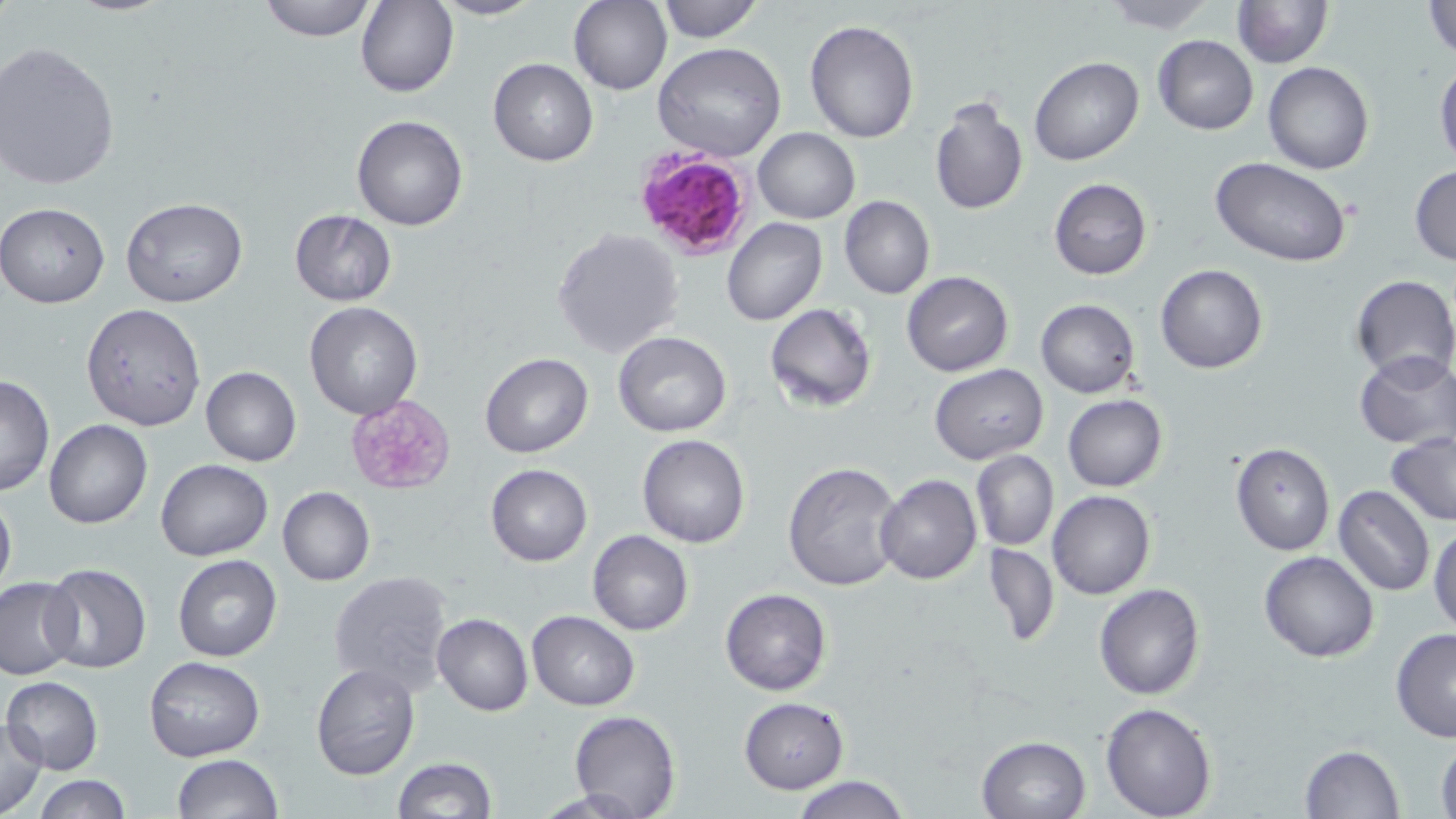
Summary:
  - Coordinate format: approximate bounding boxes as (x1,y1)-(x2,y2) corner pairs in pixels
  - Platelet locations: (345,393)-(457,492)
  - Uninfected red blood cell locations: (258,0)-(379,41), (433,0)-(542,21), (569,0)-(672,95), (656,0)-(762,42), (1096,0)-(1222,32), (1232,0)-(1332,68), (357,1)-(458,98), (1424,1)-(1454,58), (804,19)-(920,143), (1152,35)-(1258,136), (0,41)-(122,191), (652,43)-(787,163), (1029,57)-(1143,167), (487,58)-(598,166), (1435,59)-(1456,170), (1263,62)-(1374,176), (928,94)-(1028,217), (351,115)-(468,231), (752,129)-(859,224), (1209,157)-(1355,271), (1409,164)-(1456,266), (1049,178)-(1151,280), (840,196)-(935,299), (121,197)-(248,308), (1,202)-(109,308), (289,210)-(396,305), (721,217)-(827,327), (552,227)-(684,360), (1155,263)-(1267,373), (902,272)-(1013,375), (1350,274)-(1455,384), (1035,300)-(1141,400), (304,302)-(423,420), (80,303)-(207,432), (765,303)-(877,412), (613,332)-(732,437), (479,352)-(594,458), (1354,352)-(1456,450), (931,364)-(1048,465), (200,366)-(302,466), (0,375)-(54,497), (1063,394)-(1167,491), (44,420)-(152,529), (1385,433)-(1456,526), (638,434)-(749,548), (1231,443)-(1334,556), (970,449)-(1059,550), (156,459)-(272,560), (782,460)-(904,592), (486,464)-(593,566), (876,474)-(982,585), (1334,485)-(1434,596), (0,487)-(16,604), (277,487)-(375,586), (1048,490)-(1155,600), (1429,523)-(1456,635), (587,529)-(694,636), (983,541)-(1060,647), (1259,551)-(1379,662), (172,554)-(282,662), (37,564)-(153,675), (327,570)-(455,696), (0,577)-(80,677), (1094,583)-(1206,699), (720,588)-(832,695), (527,610)-(641,710), (432,613)-(532,716), (1390,629)-(1456,742), (144,655)-(266,762), (310,663)-(421,780), (2,676)-(103,774), (738,696)-(850,794), (1100,702)-(1217,818), (570,710)-(678,819), (0,717)-(48,818), (1435,732)-(1456,819), (977,735)-(1091,819), (1298,744)-(1404,819), (171,753)-(284,819), (390,757)-(497,818), (31,775)-(133,818), (792,775)-(909,819)
  - Plasmodium falciparum-infected red blood cell locations: (629,142)-(760,262)
  - Slide-level diagnosis: Plasmodium falciparum
  - Field of view: single
  - Stain: May-Grünwald-Giemsa
  - Modality: light microscopy
  - Preparation: thin blood smear
  - Magnification: 1000x
  - Image size: 1456×819 pixels